Describe the morphology of the erythrocytes.
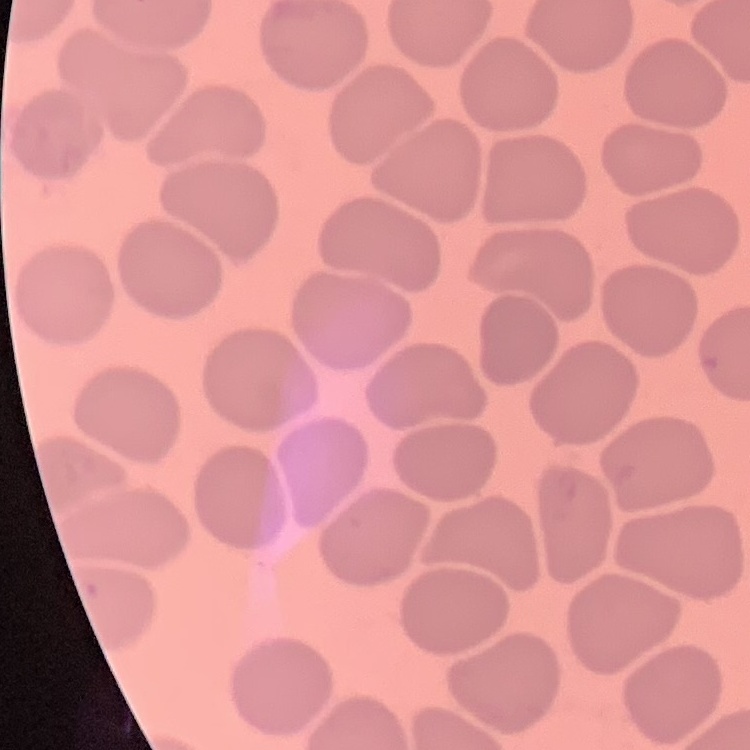

No rouleaux formation.

Thin blood smear. Stained with either Field's or Giemsa. One tile cut from a larger photomicrograph.